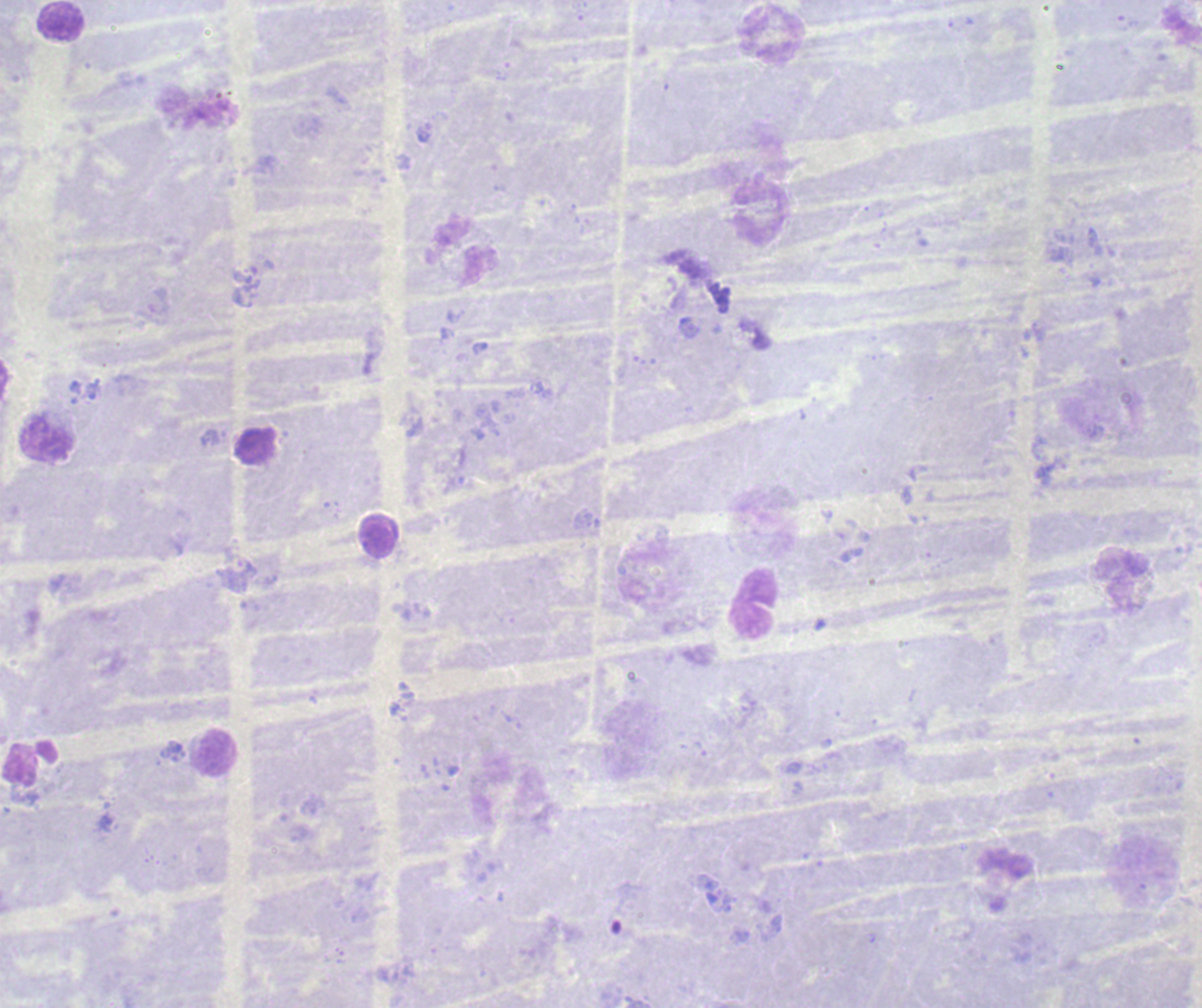

{
  "context": "previously used in a real diagnosis",
  "image_size": "1202×1008 pixels",
  "field_of_view": "single",
  "result": "negative for malaria parasites",
  "magnification": "100x",
  "leukocyte_locations": "approximate centers as (x, y) in pixels: (63, 22), (771, 35), (760, 213), (461, 252), (46, 440), (378, 536), (755, 605), (218, 754)",
  "stain": "Romanowsky",
  "background_quality": "unsatisfactory",
  "preparation": "thick blood film"
}